Outline each blood parasite and name the species.
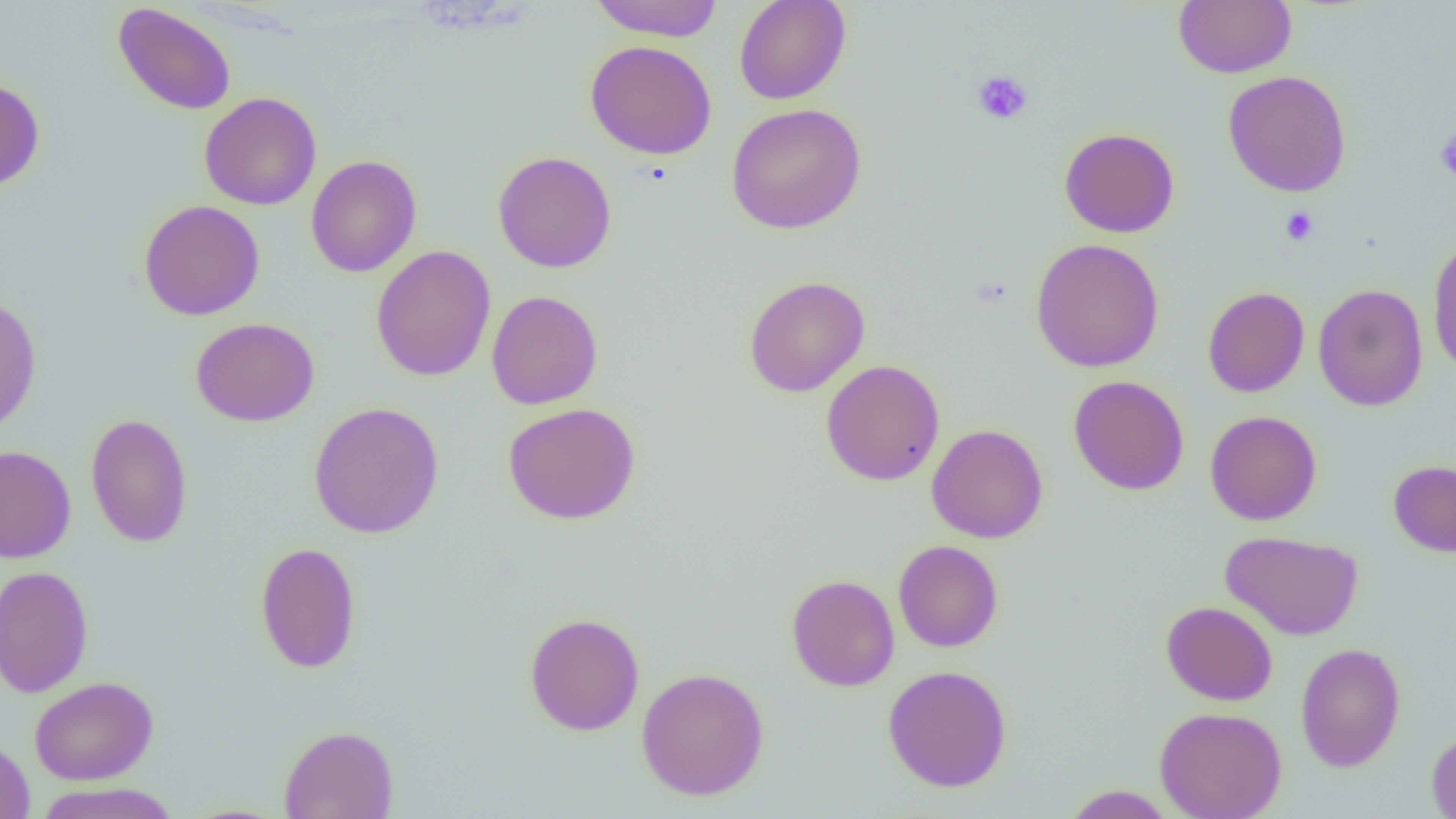
No blood parasites seen.

Summary:
  - Coordinate format: approximate bounding boxes as (x1,y1)-(x2,y2) corner pairs in pixels
  - Platelet locations: (971,70)-(1033,125), (1434,130)-(1456,180), (1280,207)-(1319,246)
  - Uninfected red blood cell locations: (588,0)-(725,41), (733,0)-(851,105), (1174,0)-(1296,78), (112,2)-(237,116), (585,40)-(717,160), (1222,70)-(1352,197), (0,77)-(45,192), (199,92)-(322,210), (726,103)-(866,234), (1059,127)-(1180,238), (492,150)-(617,273), (305,155)-(421,277), (138,200)-(265,321), (1427,236)-(1456,376), (1029,238)-(1165,373), (370,245)-(496,382), (743,276)-(870,397), (1313,284)-(1428,411), (1202,286)-(1309,397), (486,290)-(603,409), (0,293)-(42,434), (190,318)-(319,426), (821,359)-(945,486), (1068,375)-(1189,496), (308,401)-(445,539), (502,402)-(641,525), (1205,410)-(1322,525), (85,413)-(193,548), (926,424)-(1048,543), (0,445)-(76,562), (1388,459)-(1456,557), (1220,530)-(1363,641), (893,540)-(1003,652), (255,541)-(362,674), (0,565)-(94,697), (786,574)-(900,691), (1161,600)-(1277,706), (524,612)-(645,736), (1295,642)-(1406,772), (883,664)-(1012,793), (636,667)-(769,801), (29,676)-(158,785), (1155,706)-(1287,819), (278,725)-(399,819), (1426,729)-(1456,819), (0,738)-(35,819), (33,782)-(182,819), (1061,785)-(1175,818)
  - Slide-level diagnosis: negative for blood parasites
  - Image size: 1456×819 pixels
  - Field of view: one of a larger specimen
  - Preparation: thin blood smear
  - Magnification: 1000x
  - Modality: optical microscopy